Identify the parasite.
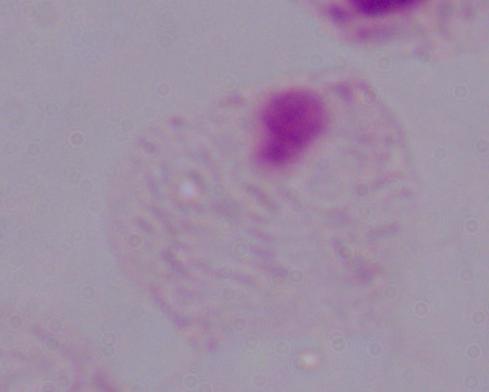
A trichomonad.

Micrograph. 1000x magnification.